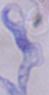

A trypanosome is seen. Micrograph. Captured at 1000x magnification.